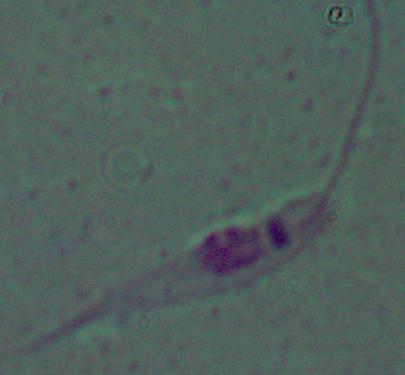
identification = Leishmania
magnification = 1000x
modality = micrograph